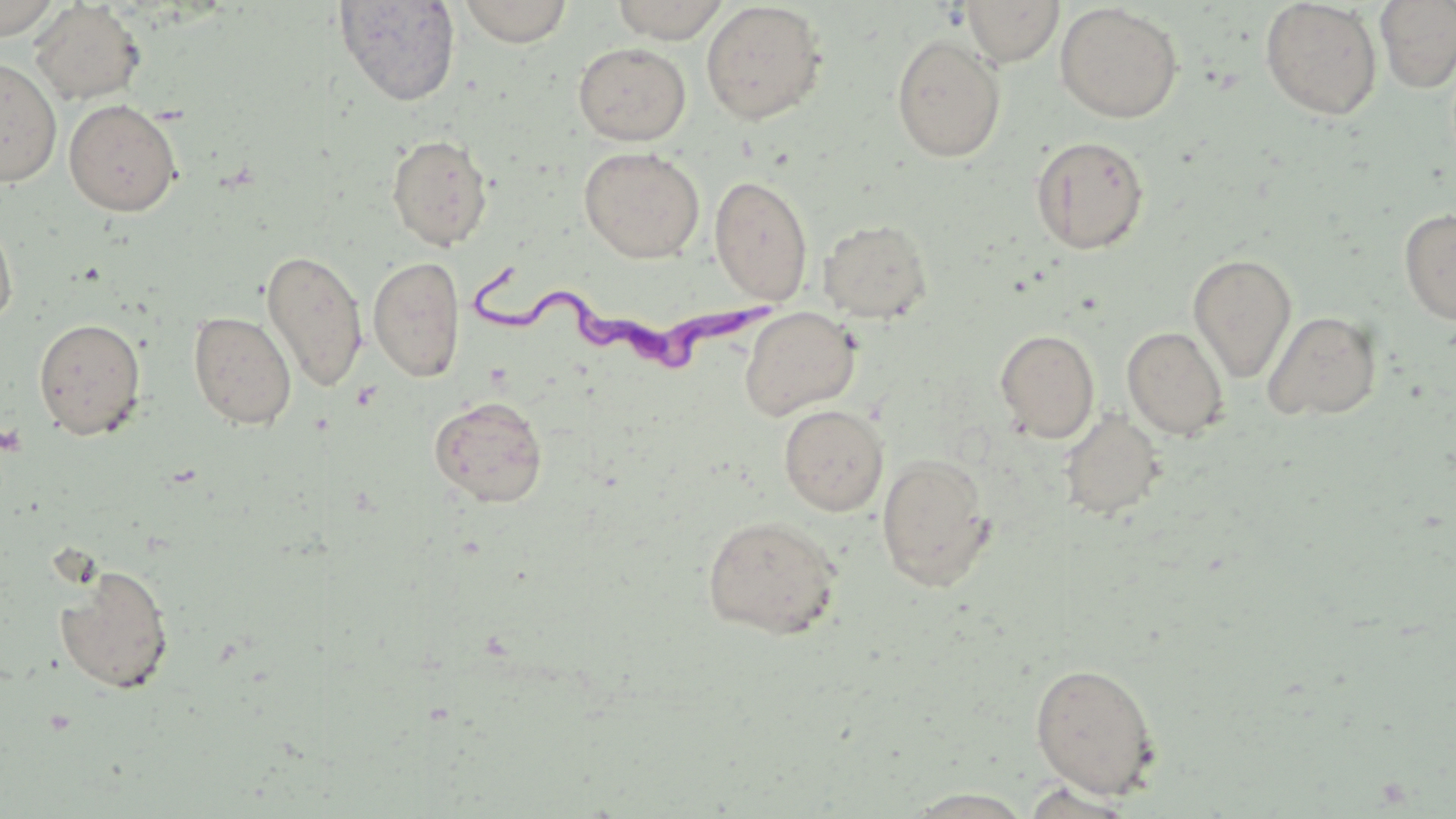
Summary:
  - Coordinate format: approximate bounding boxes as [x1, y1, x2, y2] in pixels
  - Trypanosoma brucei locations: [469, 250, 770, 372]
  - Uninfected red blood cell locations: [0, 0, 63, 40], [333, 0, 461, 107], [457, 0, 573, 47], [611, 0, 730, 43], [962, 0, 1064, 66], [1260, 0, 1383, 121], [1375, 0, 1456, 94], [700, 1, 827, 125], [29, 2, 146, 106], [1055, 2, 1183, 123], [891, 33, 1006, 163], [573, 42, 692, 146], [0, 57, 62, 187], [63, 98, 183, 216], [386, 133, 494, 251], [1030, 135, 1150, 255], [579, 146, 705, 263], [709, 173, 813, 306], [1398, 208, 1456, 325], [0, 211, 18, 329], [818, 218, 933, 324], [261, 249, 369, 392], [1188, 253, 1297, 383], [368, 256, 465, 382], [739, 307, 860, 421], [188, 310, 297, 430], [1262, 310, 1383, 421], [33, 317, 147, 440], [1122, 327, 1229, 441], [994, 329, 1100, 443], [429, 395, 548, 508], [778, 404, 889, 516], [1059, 410, 1167, 521], [876, 453, 996, 591], [701, 514, 843, 638], [55, 564, 175, 695], [1029, 661, 1161, 799], [1016, 780, 1144, 818], [900, 788, 1039, 818]
  - Slide-level diagnosis: Trypanosoma brucei
  - Preparation: thin blood film
  - Field of view: single
  - Stain: May-Grünwald-Giemsa
  - Modality: optical microscopy
  - Image size: 1456×819 pixels
  - Magnification: 1000x